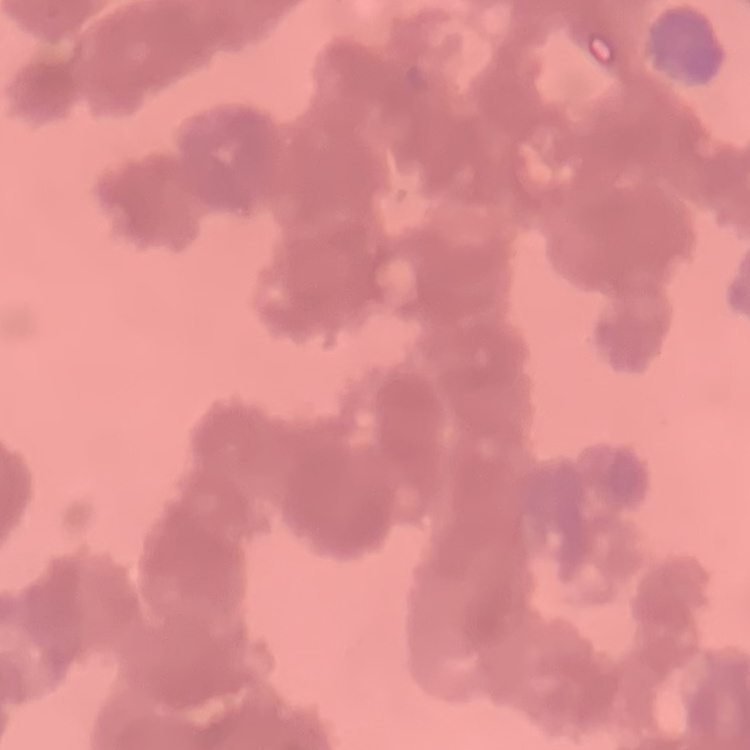 The red blood cells show rouleaux formation. Thin blood smear. One tile cut from a larger photomicrograph. Field's or Giemsa stain.